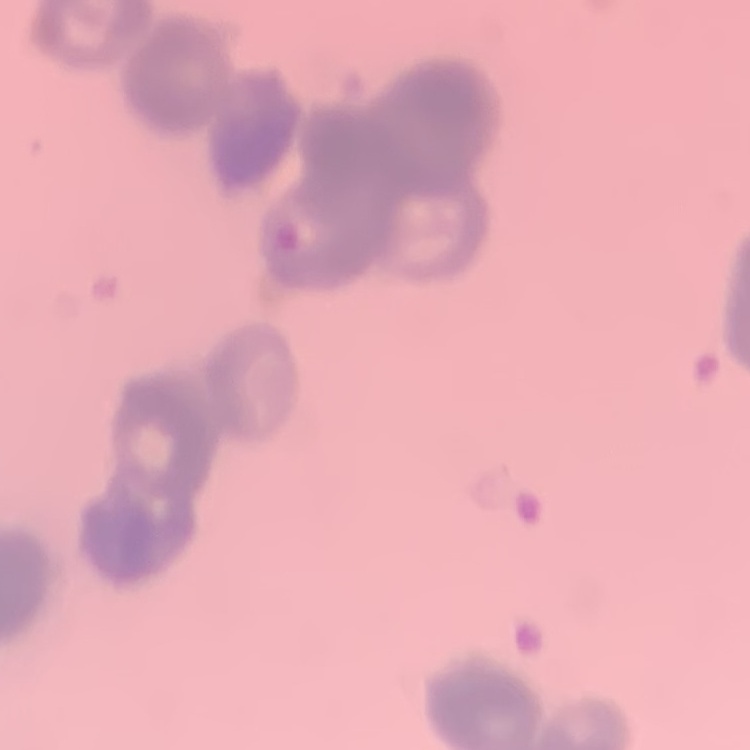
{
  "red_blood_cell_morphology": "rouleaux formation",
  "stain": "Field's or Giemsa",
  "image_type": "one tile cut from a larger photomicrograph",
  "preparation": "thin blood film"
}